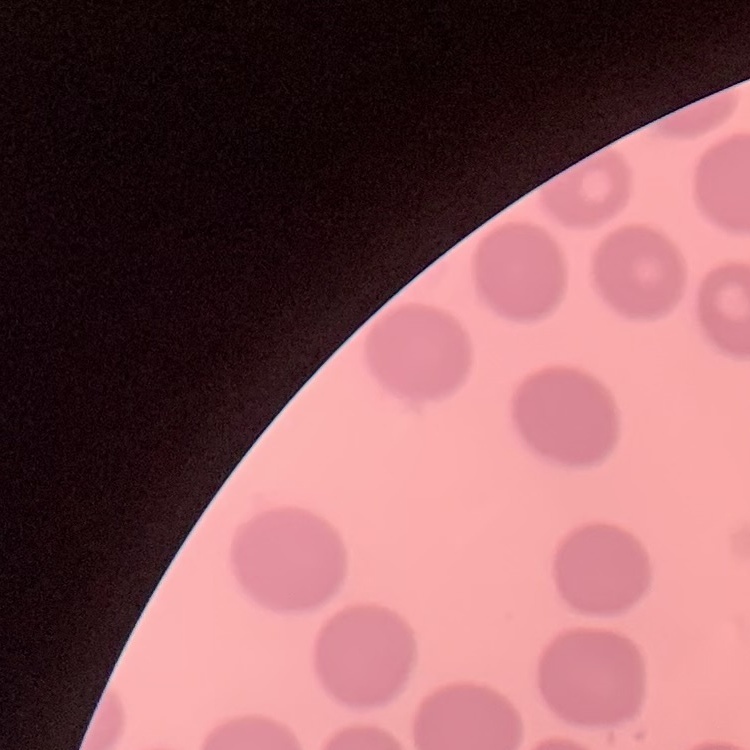
Summary:
  - Red blood cell morphology: no rouleaux formation
  - Image type: square crop of a larger photomicrograph
  - Stain: Field's or Giemsa
  - Preparation: thin blood smear